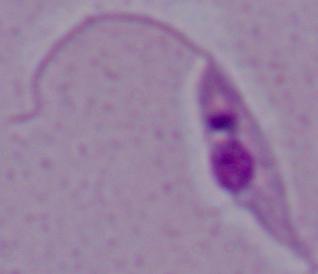
Captured at 1000x magnification. Micrograph. A Leishmania parasite is seen.